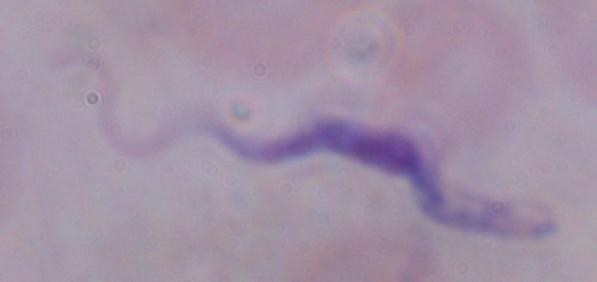
Summary:
  - Identification: trypanosome
  - Magnification: 1000x
  - Modality: photomicrograph